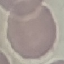

result: no malaria parasites seen
image_type: automatically extracted cell patch, resized to 64 × 64 pixels
capture: smartphone camera at the microscope eyepiece
stain: Giemsa
preparation: thin blood smear